Classify this cell by malaria status.
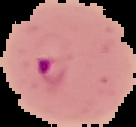

Parasitized.

Summary:
  - Preparation: thin blood film
  - Image size: 136×127 pixels
  - Image type: segmented cell region on a black background